Give the position of every Plasmodium parasite visible.
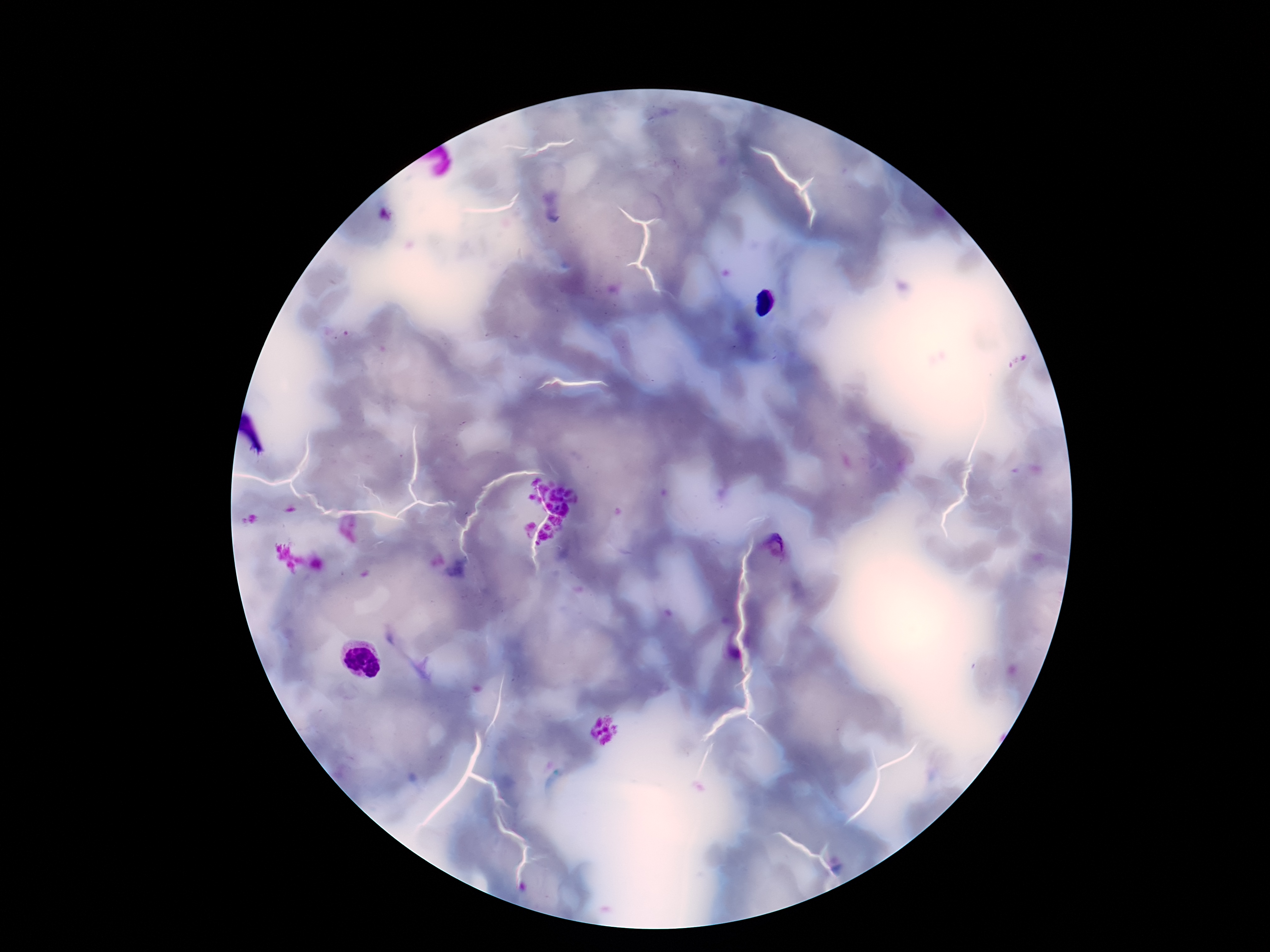

Approximate centers as {x, y} in pixels.
Plasmodium parasites: {777, 543}.

patient_malaria_status: infected
image_size: 1270×952 pixels
field_of_view: single
preparation: thick blood film
capture: smartphone camera through the microscope eyepiece
stain: Giemsa
magnification: 100x